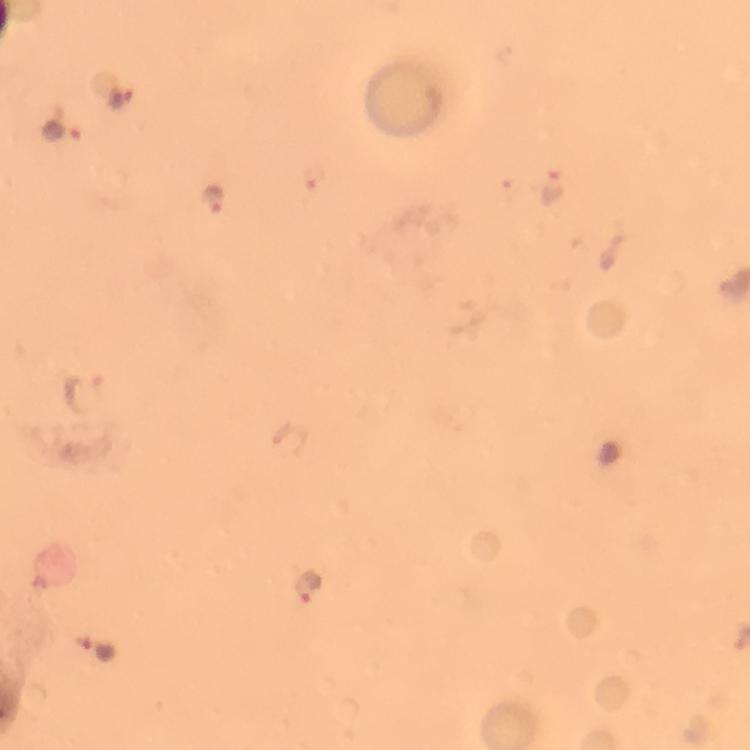
Approximate centers as (x, y) in pixels.
Summary:
  - Malaria parasite locations: (122, 97), (62, 133), (316, 176), (550, 185), (217, 197), (84, 392), (309, 586), (98, 648)
  - Context: from a malaria diagnostic workup
  - Image size: 750×750 pixels
  - Immersion oil: applied
  - Cropped from: a single field of view
  - Stain: Giemsa
  - Capture: smartphone mounted on the microscope
  - Preparation: thick smear
  - Magnification: 100x